Describe the morphology of the erythrocytes.
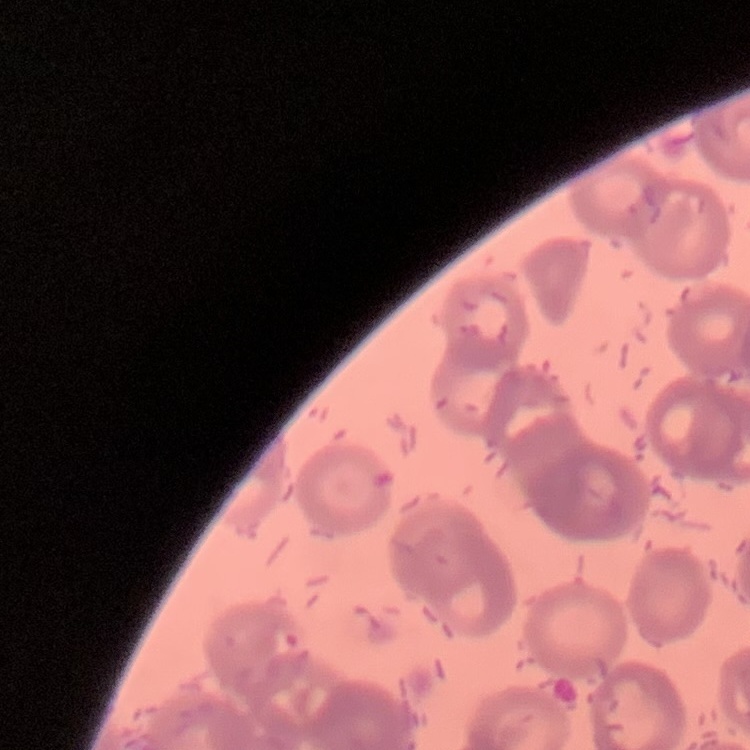
Rouleaux formation.

preparation = thin blood film
image type = one tile cut from a larger photomicrograph
stain = Field's or Giemsa